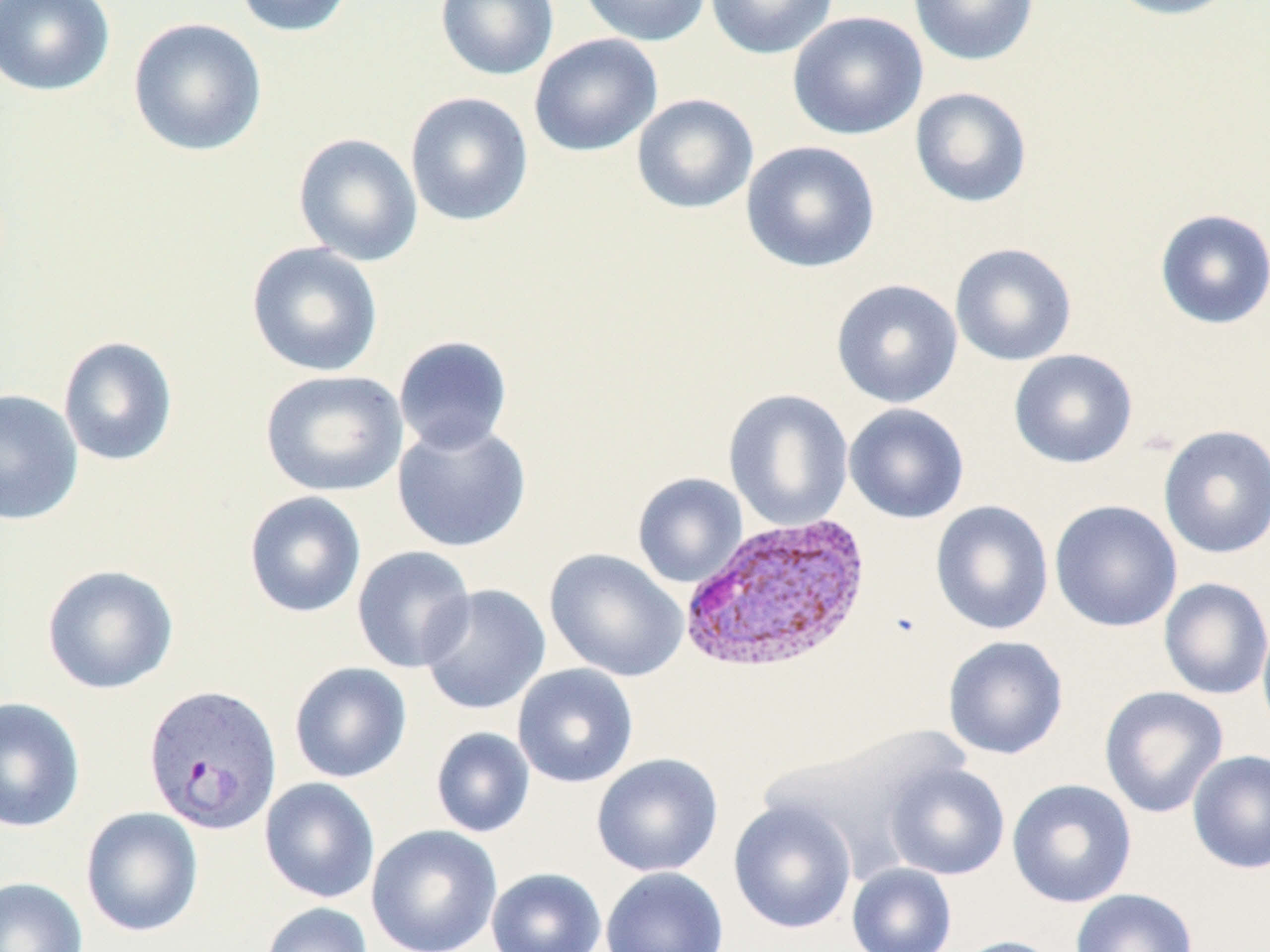 Approximate bounding boxes as [x1, y1, x2, y2] in pixels. Plasmodium vivax-infected red blood cell locations: [678, 515, 873, 676], [142, 684, 282, 836]. Uninfected red blood cell locations: [0, 0, 116, 97], [233, 0, 354, 38], [435, 0, 559, 81], [576, 0, 711, 47], [705, 0, 838, 59], [907, 0, 1039, 66], [1103, 0, 1243, 21], [787, 11, 928, 141], [127, 17, 267, 158], [529, 34, 663, 157], [909, 86, 1033, 208], [405, 91, 534, 227], [631, 93, 759, 214], [293, 132, 423, 266], [741, 140, 881, 274], [1154, 208, 1270, 330], [246, 242, 384, 377], [949, 242, 1077, 366], [830, 278, 963, 409], [392, 335, 513, 454], [57, 336, 179, 467], [1008, 349, 1138, 469], [259, 369, 408, 497], [0, 389, 84, 526], [723, 389, 854, 531], [844, 403, 969, 524], [391, 420, 533, 553], [1158, 425, 1270, 559], [632, 472, 748, 588], [243, 491, 366, 619], [1049, 499, 1182, 633], [930, 500, 1054, 635], [351, 545, 477, 673], [544, 548, 689, 682], [41, 564, 179, 695], [1159, 577, 1270, 700], [418, 584, 551, 715], [1257, 614, 1270, 741], [943, 635, 1069, 760], [288, 661, 412, 783], [512, 664, 639, 788], [1099, 686, 1229, 818], [0, 697, 85, 833], [430, 726, 535, 838], [1187, 749, 1270, 875], [591, 753, 724, 877], [884, 762, 1010, 880], [259, 777, 380, 903], [1007, 778, 1137, 908], [728, 799, 857, 934], [80, 806, 204, 937], [366, 825, 502, 952], [846, 862, 957, 952], [601, 866, 729, 952], [486, 867, 607, 952], [0, 876, 88, 952], [1071, 888, 1197, 952], [261, 902, 373, 952], [951, 936, 1064, 952]. Slide-level diagnosis: Plasmodium vivax. Light microscopy. May-Grünwald-Giemsa-stained preparation. Image is 1270×952 pixels. Captured at 1000x magnification. One field of a larger specimen. Thin blood film.